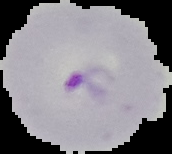
The area outside the segmented cell region is set to black. Image is 172×154 pixels. From a thin blood film. Result: malaria parasites detected.